State which parasite is depicted.
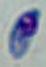

This is Toxoplasma gondii.

{
  "magnification": "1000x",
  "modality": "micrograph"
}